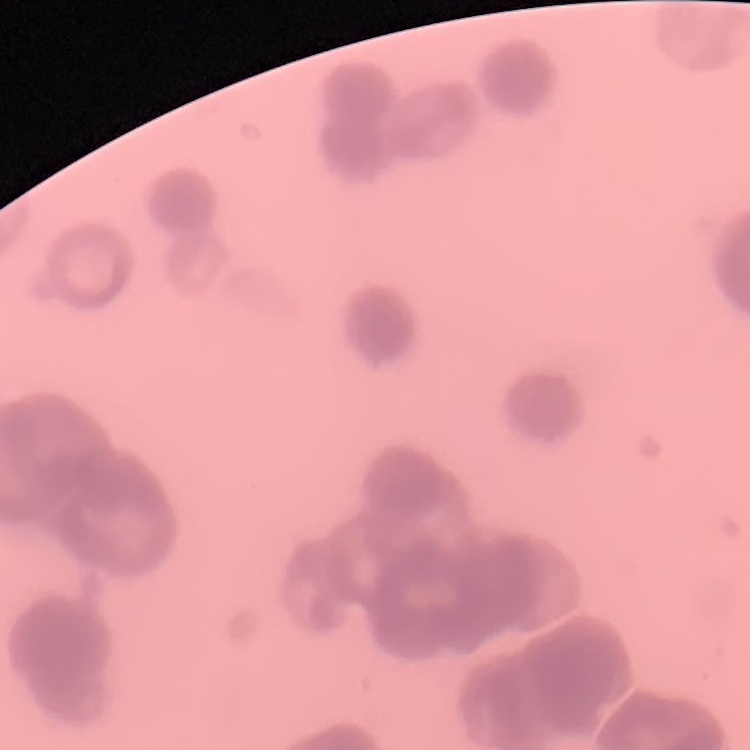

The erythrocytes show rouleaux formation. Thin blood smear. Stained with either Field's or Giemsa. One tile cut from a larger photomicrograph.